Identify the parasite.
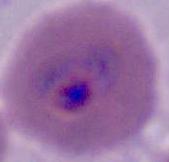
This is Plasmodium.

Summary:
  - Magnification: 400x or 1000x
  - Modality: micrograph